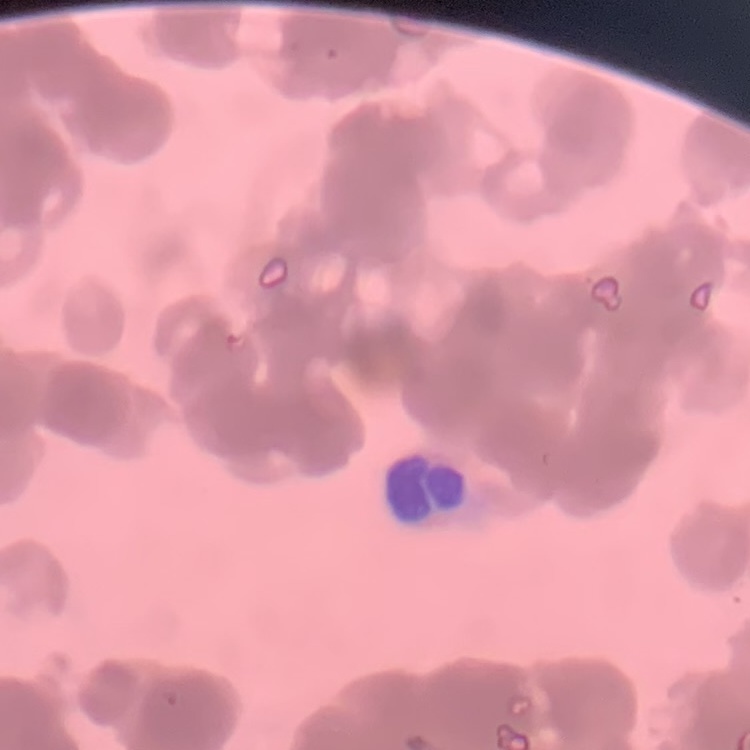

The red blood cells show rouleaux formation. Square crop of a larger photomicrograph. Thin blood film. Field's or Giemsa stain.